Assess this cell for malaria.
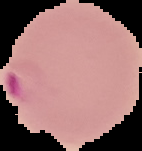
It is parasitized.

Segmented cell region on a black background. Image is 142×151 pixels. From a thin blood smear.